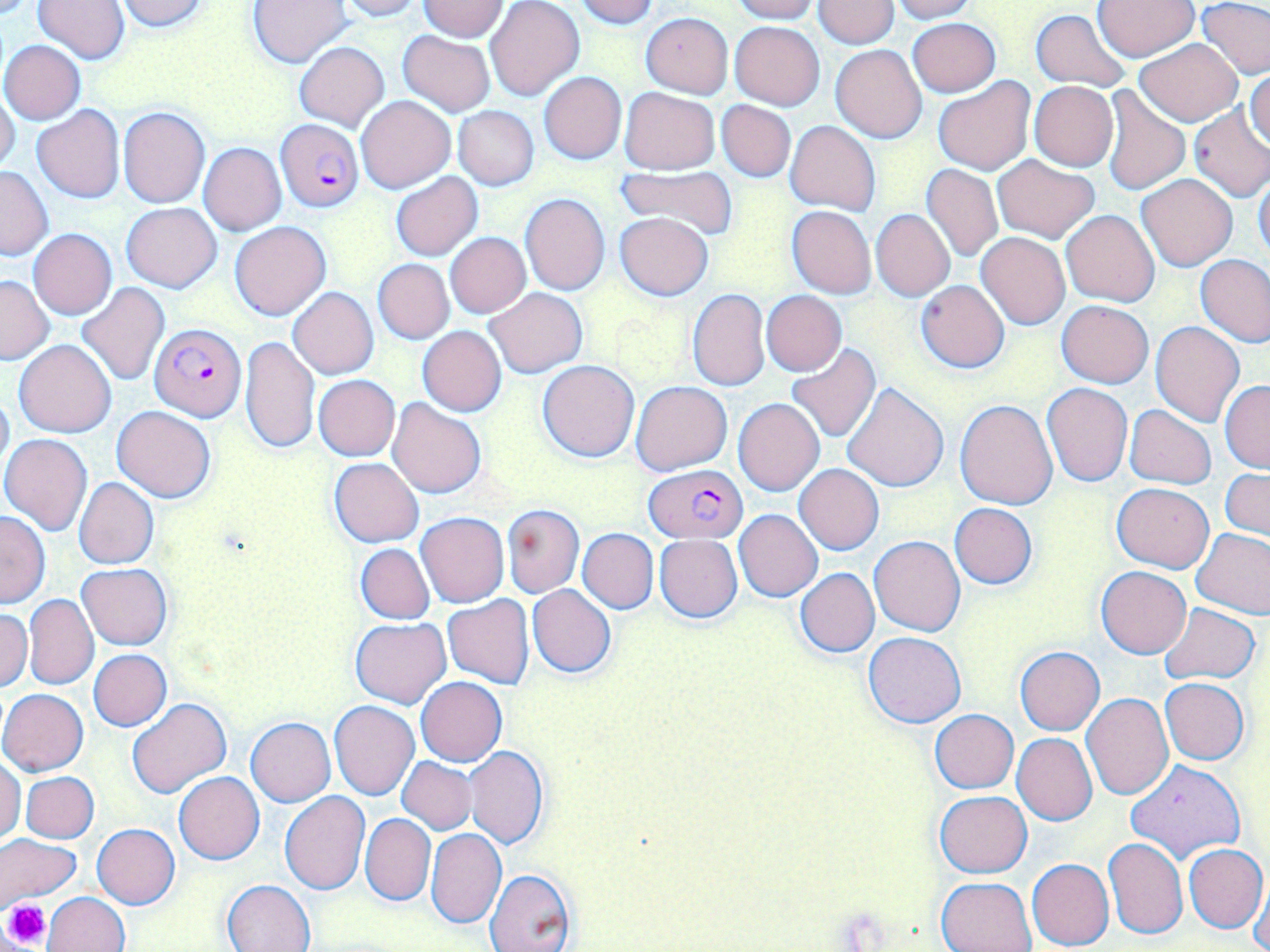
Approximate bounding boxes as (x1,y1)-(x2,y2) corner pairs in pixels. Platelet locations: (1,898)-(51,949). Uninfected red blood cell locations: (34,0)-(130,64), (114,0)-(214,33), (247,0)-(352,68), (332,0)-(425,21), (572,0)-(659,27), (726,0)-(818,22), (888,0)-(975,22), (1197,0)-(1270,80), (417,1)-(508,41), (486,1)-(584,102), (813,1)-(898,49), (1093,1)-(1198,60), (1031,9)-(1131,93), (640,13)-(733,97), (909,18)-(1000,97), (729,21)-(824,109), (398,30)-(496,118), (1134,38)-(1242,126), (1,40)-(86,124), (293,42)-(389,130), (831,45)-(927,142), (1245,67)-(1270,153), (539,71)-(626,163), (934,77)-(1035,175), (1029,81)-(1119,171), (619,87)-(719,174), (0,88)-(20,173), (1101,88)-(1190,197), (356,95)-(456,194), (717,100)-(796,182), (31,106)-(124,203), (453,106)-(539,189), (117,107)-(210,208), (1187,107)-(1270,203), (785,120)-(881,216), (199,143)-(286,235), (992,154)-(1100,244), (922,162)-(1002,263), (0,166)-(52,260), (615,166)-(739,241), (1253,170)-(1270,262), (390,173)-(483,261), (1137,174)-(1237,270), (519,192)-(609,295), (122,203)-(221,294), (787,206)-(876,298), (870,209)-(955,302), (1060,209)-(1160,307), (614,211)-(715,301), (230,221)-(331,320), (28,229)-(117,319), (445,232)-(530,318), (977,233)-(1069,329), (1195,253)-(1270,348), (373,259)-(454,343), (1,276)-(54,365), (916,280)-(1010,374), (76,284)-(171,388), (288,287)-(378,379), (485,288)-(587,378), (686,288)-(770,392), (761,291)-(847,375), (1057,301)-(1153,387), (1151,321)-(1244,427), (417,326)-(507,416), (240,336)-(320,455), (13,340)-(116,437), (785,345)-(882,442), (537,360)-(639,462), (313,375)-(400,461), (1220,380)-(1270,473), (632,381)-(732,475), (1043,383)-(1132,486), (0,384)-(14,478), (843,384)-(949,492), (388,397)-(486,498), (734,398)-(825,495), (955,399)-(1058,510), (112,405)-(216,502), (1125,405)-(1216,489), (0,434)-(93,535), (328,457)-(425,548), (794,464)-(884,554), (1221,469)-(1269,542), (74,477)-(158,570), (1112,483)-(1213,573), (950,503)-(1038,588), (503,504)-(584,597), (735,510)-(822,601), (0,511)-(49,607), (417,512)-(509,607), (577,529)-(658,612), (1191,529)-(1270,619), (654,535)-(742,623), (869,535)-(966,636), (356,543)-(434,625), (76,562)-(173,650), (1096,566)-(1191,659), (794,568)-(879,658), (527,586)-(616,677), (22,593)-(99,690), (442,596)-(534,690), (1159,603)-(1261,684), (0,609)-(32,692), (351,617)-(450,708), (863,631)-(966,728), (1014,647)-(1104,735), (89,649)-(172,730), (416,677)-(508,766), (1160,678)-(1250,765), (0,689)-(88,776), (1081,692)-(1174,801), (128,698)-(231,800), (330,701)-(420,800), (929,710)-(1019,793), (245,717)-(336,806), (1012,734)-(1097,825), (464,746)-(549,849), (396,757)-(477,835), (0,758)-(25,845), (1125,761)-(1246,865), (20,771)-(98,843), (174,772)-(264,865), (934,791)-(1032,878), (279,793)-(370,895), (360,814)-(435,905), (92,823)-(179,909), (426,828)-(507,929), (0,834)-(82,908), (1104,838)-(1188,940), (1184,844)-(1268,933), (1027,857)-(1114,950), (483,866)-(577,952), (1247,871)-(1269,952), (935,876)-(1038,951), (223,879)-(316,952), (44,892)-(128,952). Plasmodium falciparum-infected red blood cell locations: (275,119)-(364,211), (150,324)-(245,420), (644,465)-(746,542). Slide-level diagnosis: Plasmodium falciparum. Optical microscopy. One field of a larger specimen. 1000x magnification. May-Grünwald-Giemsa-stained preparation. Image is 1270×952 pixels. Thin blood smear.